Assess the morphology of the red blood cells.
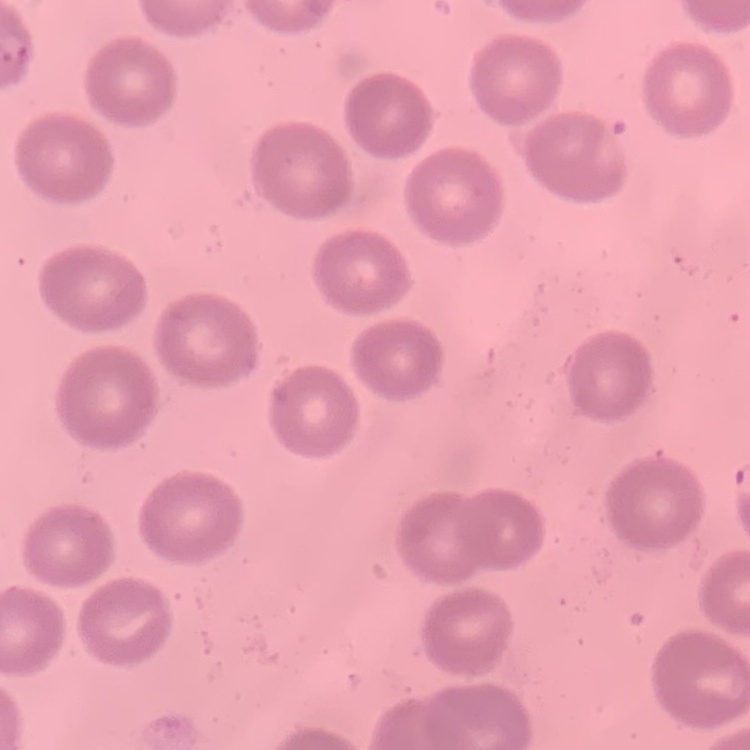

No rouleaux formation.

{
  "stain": "Field's or Giemsa",
  "image_type": "square crop of a larger photomicrograph",
  "preparation": "thin blood film"
}